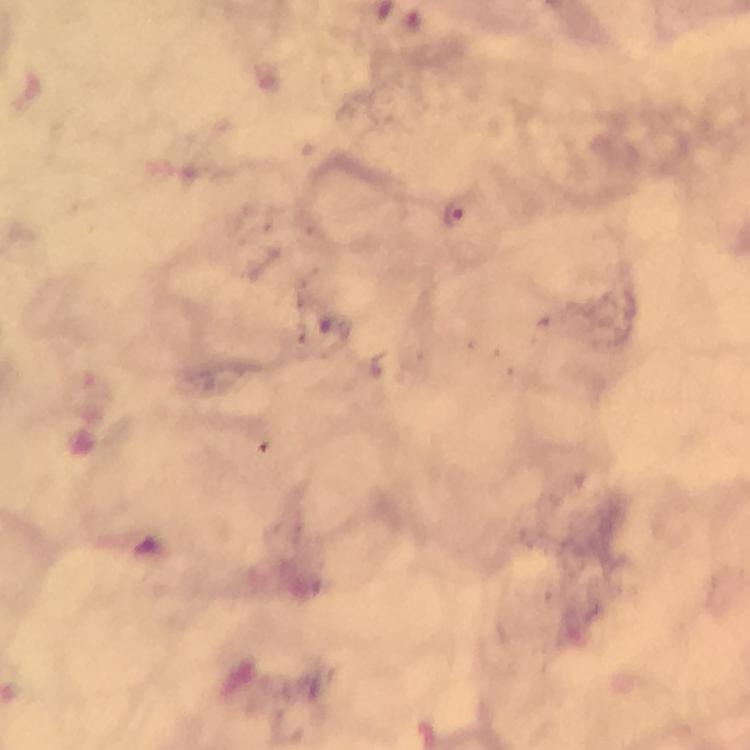
stain = Giemsa
context = from a malaria diagnostic workup
capture = smartphone mounted on the microscope
malaria parasite locations = approximate object centers, in pixels from the top-left corner: (x=452, y=212)
cropped from = a single field of view
magnification = 100x
image size = 750×750 pixels
preparation = thick smear
immersion oil = applied